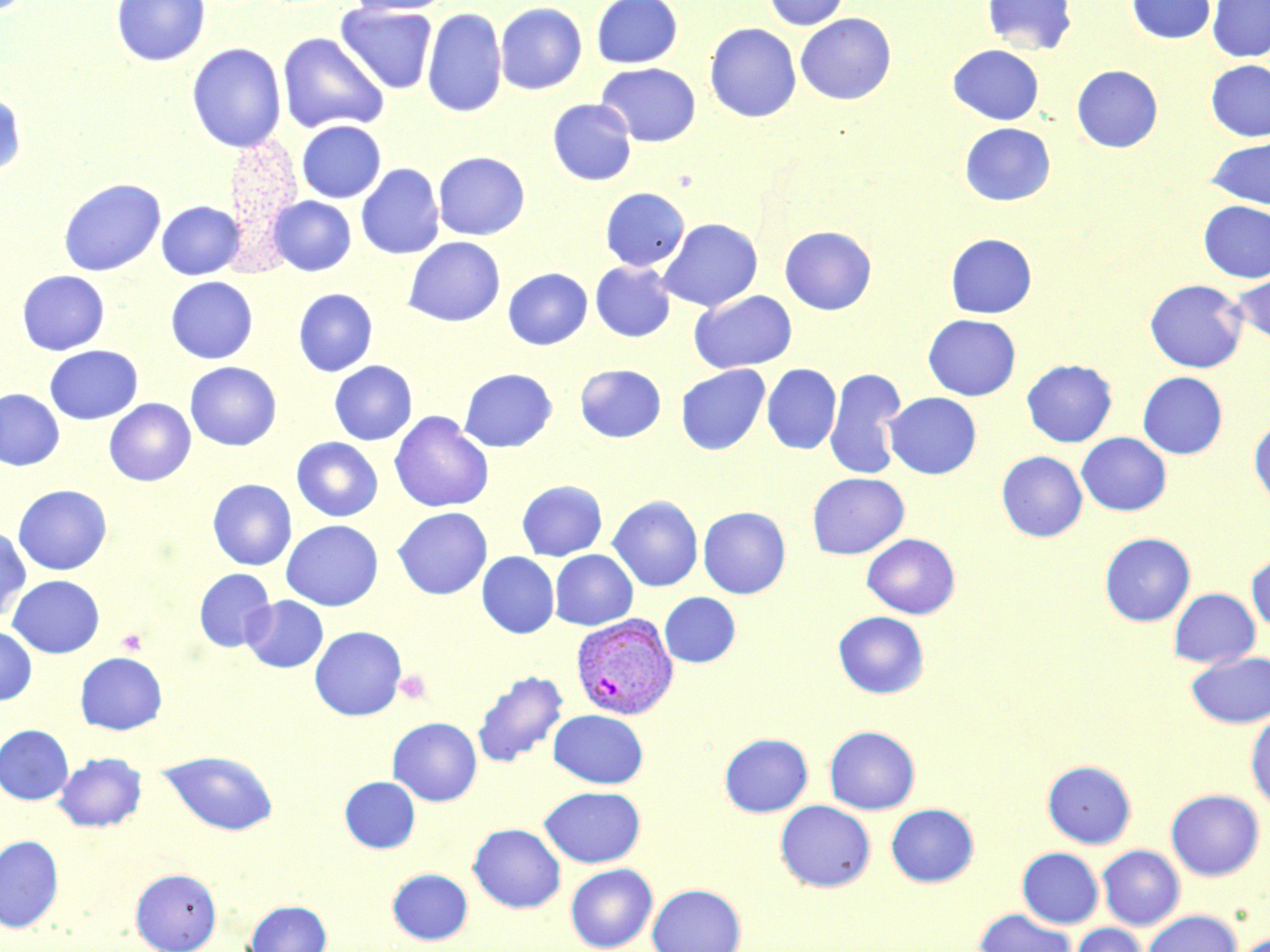
Approximate bounding boxes as [x1, y1, x2, y2] in pixels. Platelet locations: [117, 629, 146, 655], [395, 669, 431, 705]. Plasmodium vivax-infected red blood cell locations: [570, 612, 678, 720]. Uninfected red blood cell locations: [111, 0, 211, 67], [342, 0, 457, 16], [591, 0, 683, 69], [762, 0, 849, 31], [981, 0, 1077, 55], [1127, 0, 1215, 43], [1207, 0, 1270, 61], [495, 2, 587, 95], [496, 2, 683, 79], [336, 4, 437, 94], [422, 7, 507, 118], [795, 13, 897, 105], [704, 23, 801, 123], [277, 32, 390, 134], [187, 43, 286, 153], [948, 44, 1044, 125], [1206, 60, 1270, 141], [596, 62, 701, 147], [1071, 65, 1163, 153], [0, 92, 26, 178], [547, 99, 637, 185], [296, 120, 386, 202], [959, 122, 1055, 206], [1207, 137, 1269, 209], [433, 151, 530, 240], [356, 163, 444, 259], [58, 178, 166, 276], [600, 187, 689, 270], [267, 196, 356, 276], [156, 200, 246, 280], [1198, 201, 1270, 282], [657, 218, 763, 312], [779, 226, 877, 315], [945, 234, 1037, 319], [404, 237, 505, 327], [590, 261, 676, 342], [503, 268, 592, 350], [17, 270, 109, 355], [1231, 271, 1270, 344], [165, 276, 258, 364], [1144, 279, 1247, 373], [293, 288, 378, 376], [689, 290, 797, 373], [923, 314, 1021, 400], [44, 345, 143, 424], [1021, 359, 1117, 447], [329, 360, 417, 445], [185, 362, 281, 451], [575, 363, 666, 442], [762, 363, 841, 454], [675, 365, 770, 455], [459, 368, 557, 453], [824, 368, 907, 480], [1138, 372, 1227, 459], [0, 389, 65, 470], [884, 392, 981, 479], [105, 398, 195, 486], [389, 411, 494, 512], [1249, 420, 1270, 507], [1077, 432, 1171, 516], [291, 437, 383, 522], [996, 451, 1087, 542], [807, 472, 909, 559], [207, 479, 297, 570], [517, 480, 607, 560], [13, 485, 111, 575], [607, 495, 703, 591], [698, 506, 791, 598], [392, 507, 492, 599], [281, 520, 383, 611], [0, 526, 32, 622], [1099, 532, 1195, 626], [861, 533, 960, 619], [550, 549, 637, 630], [1246, 551, 1270, 634], [477, 552, 559, 638], [194, 568, 276, 652], [8, 574, 105, 658], [1169, 588, 1260, 667], [660, 592, 740, 668], [242, 595, 328, 674], [833, 611, 929, 699], [0, 625, 37, 705], [309, 626, 407, 721], [1186, 651, 1270, 728], [75, 652, 167, 735], [471, 670, 568, 769], [549, 709, 648, 788], [1246, 712, 1270, 813], [387, 717, 482, 806], [0, 725, 73, 804], [824, 725, 920, 814], [719, 733, 813, 817], [159, 750, 279, 835], [54, 752, 147, 832], [1042, 760, 1136, 848], [340, 776, 420, 853], [539, 786, 645, 867], [1166, 789, 1264, 880], [775, 800, 876, 892], [886, 803, 979, 887], [468, 823, 566, 913], [0, 835, 64, 932], [1097, 845, 1185, 930], [1017, 847, 1104, 928], [565, 864, 658, 952], [130, 868, 222, 952], [387, 868, 473, 945], [647, 883, 746, 952], [244, 900, 331, 952], [973, 908, 1076, 952], [1143, 910, 1241, 952], [1070, 924, 1148, 952], [1230, 932, 1270, 952]. Slide-level diagnosis: Plasmodium vivax. Single field of view. Thin blood film. 1000x magnification. Light microscopy. Image is 1270×952 pixels. May-Grünwald-Giemsa stain.